Locate and identify every blood parasite.
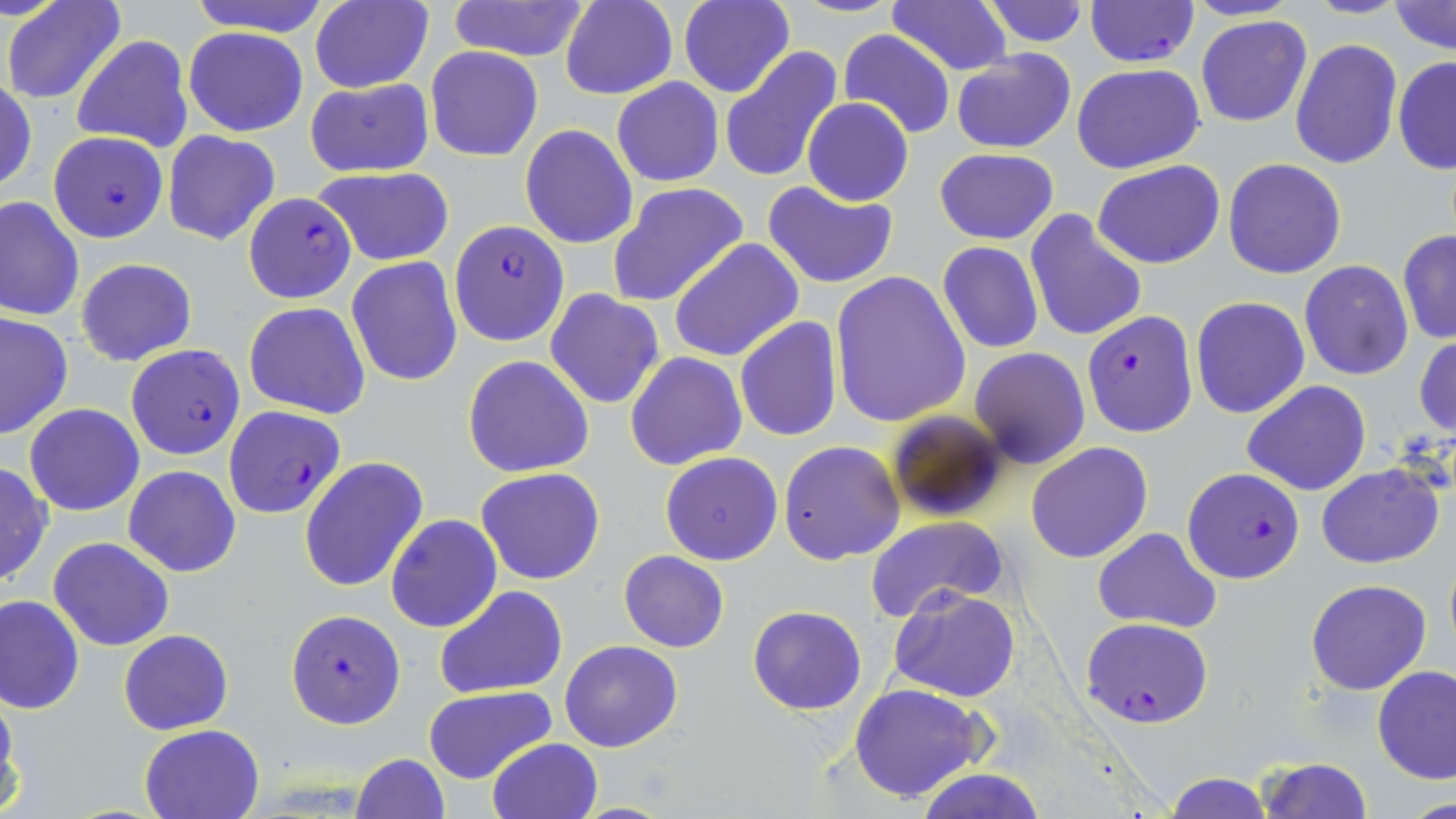
Approximate bounding boxes as named x1/y1/x2/y2 corners in pixels.
Plasmodium falciparum-infected red blood cells: (x1=1083, y1=0, x2=1198, y2=68), (x1=47, y1=131, x2=168, y2=243), (x1=242, y1=192, x2=356, y2=303), (x1=449, y1=219, x2=569, y2=347), (x1=1081, y1=310, x2=1198, y2=436), (x1=125, y1=343, x2=246, y2=460), (x1=222, y1=405, x2=345, y2=520), (x1=1182, y1=467, x2=1304, y2=584), (x1=286, y1=608, x2=405, y2=729), (x1=1081, y1=617, x2=1215, y2=728).
No Plasmodium ovale, Plasmodium malariae, Plasmodium vivax, Babesia divergens, or Trypanosoma brucei observed.

Uninfected red blood cell locations: (x1=3, y1=0, x2=126, y2=105), (x1=185, y1=0, x2=332, y2=37), (x1=309, y1=0, x2=434, y2=94), (x1=445, y1=0, x2=592, y2=64), (x1=559, y1=0, x2=678, y2=100), (x1=787, y1=0, x2=906, y2=18), (x1=886, y1=0, x2=1014, y2=76), (x1=979, y1=0, x2=1090, y2=46), (x1=1307, y1=0, x2=1408, y2=19), (x1=677, y1=1, x2=796, y2=99), (x1=1390, y1=1, x2=1454, y2=54), (x1=1195, y1=15, x2=1313, y2=127), (x1=183, y1=27, x2=308, y2=136), (x1=838, y1=29, x2=957, y2=137), (x1=71, y1=34, x2=194, y2=154), (x1=1289, y1=38, x2=1402, y2=170), (x1=425, y1=46, x2=543, y2=162), (x1=719, y1=47, x2=844, y2=184), (x1=950, y1=49, x2=1077, y2=153), (x1=1392, y1=55, x2=1455, y2=175), (x1=1071, y1=63, x2=1206, y2=173), (x1=0, y1=76, x2=36, y2=197), (x1=304, y1=77, x2=435, y2=178), (x1=612, y1=77, x2=723, y2=187), (x1=802, y1=98, x2=913, y2=207), (x1=519, y1=124, x2=638, y2=249), (x1=162, y1=130, x2=280, y2=246), (x1=935, y1=147, x2=1058, y2=244), (x1=1223, y1=158, x2=1346, y2=278), (x1=1093, y1=160, x2=1225, y2=269), (x1=312, y1=167, x2=456, y2=267), (x1=762, y1=180, x2=899, y2=288), (x1=607, y1=182, x2=749, y2=308), (x1=1, y1=195, x2=84, y2=322), (x1=1023, y1=209, x2=1148, y2=343), (x1=1396, y1=230, x2=1456, y2=345), (x1=667, y1=239, x2=804, y2=363), (x1=937, y1=241, x2=1044, y2=354), (x1=347, y1=256, x2=463, y2=388), (x1=75, y1=257, x2=197, y2=366), (x1=1298, y1=260, x2=1414, y2=381), (x1=829, y1=271, x2=970, y2=428), (x1=545, y1=290, x2=664, y2=408), (x1=1189, y1=296, x2=1310, y2=419), (x1=245, y1=302, x2=370, y2=420), (x1=0, y1=310, x2=73, y2=440), (x1=735, y1=317, x2=843, y2=441), (x1=1414, y1=333, x2=1456, y2=439), (x1=970, y1=347, x2=1090, y2=469), (x1=625, y1=352, x2=747, y2=472), (x1=463, y1=355, x2=594, y2=476), (x1=1242, y1=380, x2=1370, y2=496), (x1=23, y1=404, x2=144, y2=515), (x1=884, y1=408, x2=1011, y2=524), (x1=779, y1=440, x2=906, y2=565), (x1=1026, y1=442, x2=1153, y2=563), (x1=660, y1=451, x2=783, y2=566), (x1=299, y1=456, x2=429, y2=594), (x1=0, y1=461, x2=52, y2=588), (x1=1316, y1=463, x2=1445, y2=568), (x1=123, y1=466, x2=241, y2=576), (x1=476, y1=467, x2=605, y2=585), (x1=385, y1=515, x2=502, y2=632), (x1=865, y1=515, x2=1008, y2=621), (x1=1092, y1=527, x2=1221, y2=635), (x1=48, y1=535, x2=175, y2=651), (x1=618, y1=550, x2=729, y2=652), (x1=1305, y1=579, x2=1432, y2=695), (x1=436, y1=587, x2=567, y2=697), (x1=889, y1=587, x2=1020, y2=701), (x1=1, y1=595, x2=84, y2=715), (x1=747, y1=606, x2=867, y2=714), (x1=118, y1=629, x2=235, y2=735), (x1=559, y1=640, x2=682, y2=752), (x1=1372, y1=665, x2=1456, y2=783), (x1=847, y1=683, x2=991, y2=803), (x1=0, y1=684, x2=19, y2=810), (x1=423, y1=687, x2=555, y2=784), (x1=139, y1=724, x2=264, y2=819), (x1=486, y1=737, x2=603, y2=819), (x1=352, y1=753, x2=450, y2=819), (x1=1254, y1=758, x2=1374, y2=817), (x1=914, y1=767, x2=1046, y2=819), (x1=1162, y1=773, x2=1273, y2=818), (x1=1410, y1=792, x2=1456, y2=818). Slide-level diagnosis: Plasmodium falciparum. May-Grünwald-Giemsa-stained preparation. Image is 1456×819 pixels. Single field of view. Optical microscopy. Thin blood film. 1000x magnification.